Report the malaria status of this cell.
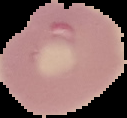
It is parasitized.

image type = segmented cell region with the area outside set to black
preparation = thin blood film
image size = 127×118 pixels